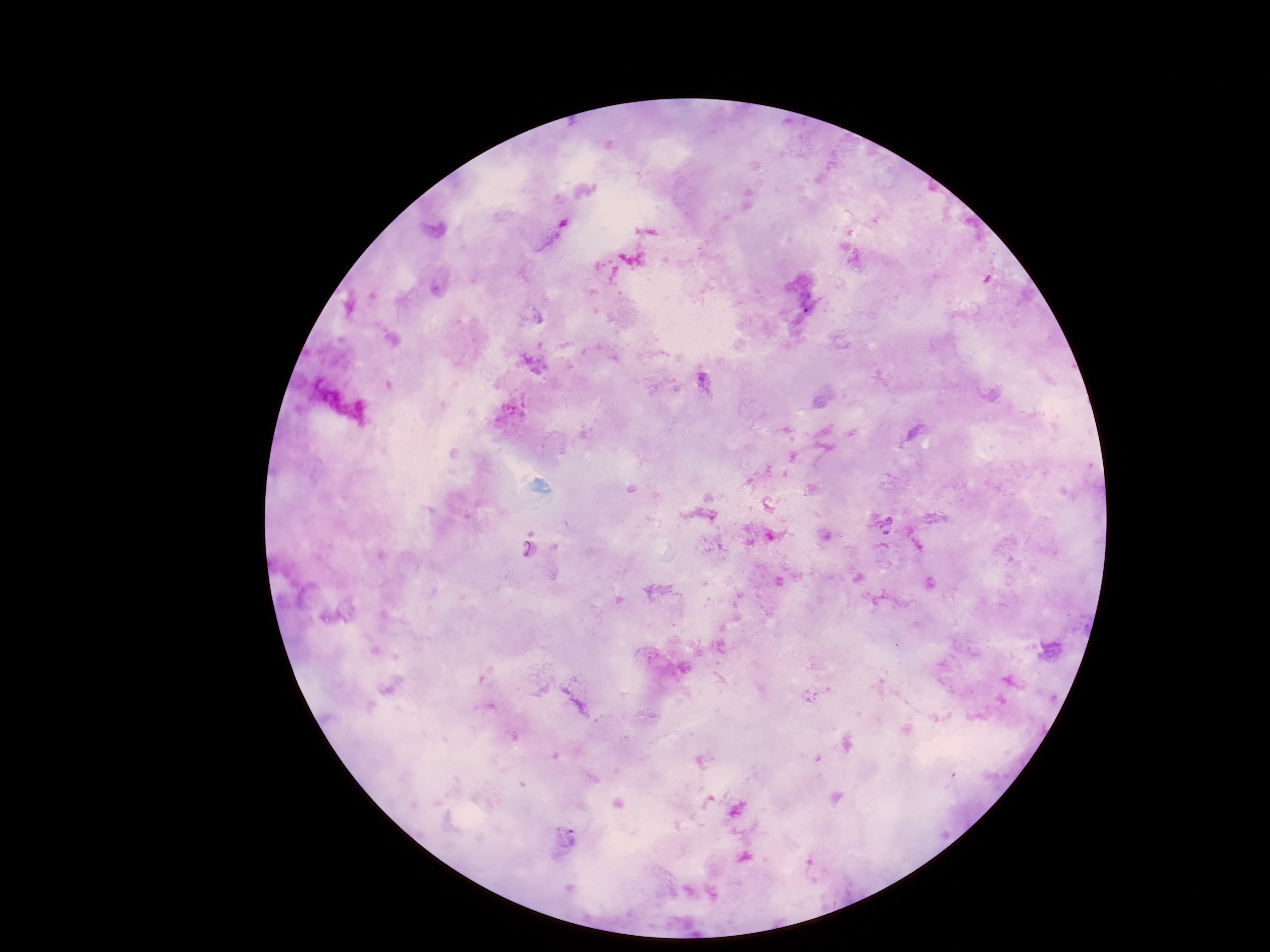

Approximate centers as (x, y) in pixels. Plasmodium parasite locations: (888, 525), (530, 549). One field from this slide. Patient malaria status: positive. 100x magnification. Image is 1270×952 pixels. Giemsa-stained preparation. Thick peripheral-blood smear. Smartphone photograph taken through the microscope eyepiece.